Comment on the morphology of the erythrocytes.
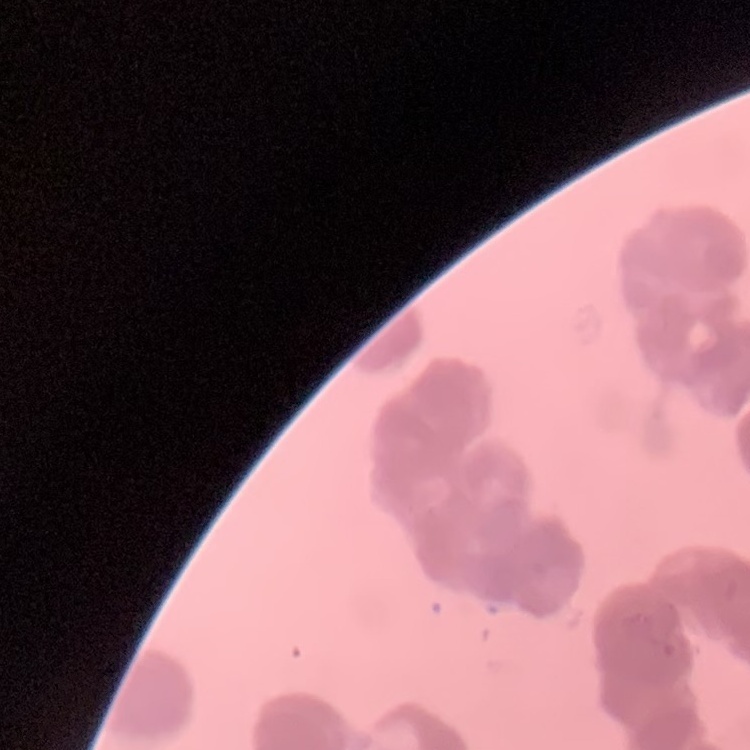

Rouleaux formation.

{
  "image_type": "square crop of a larger photomicrograph",
  "stain": "Field's or Giemsa",
  "preparation": "thin blood smear"
}